Outline each Plasmodium falciparum-infected red blood cell.
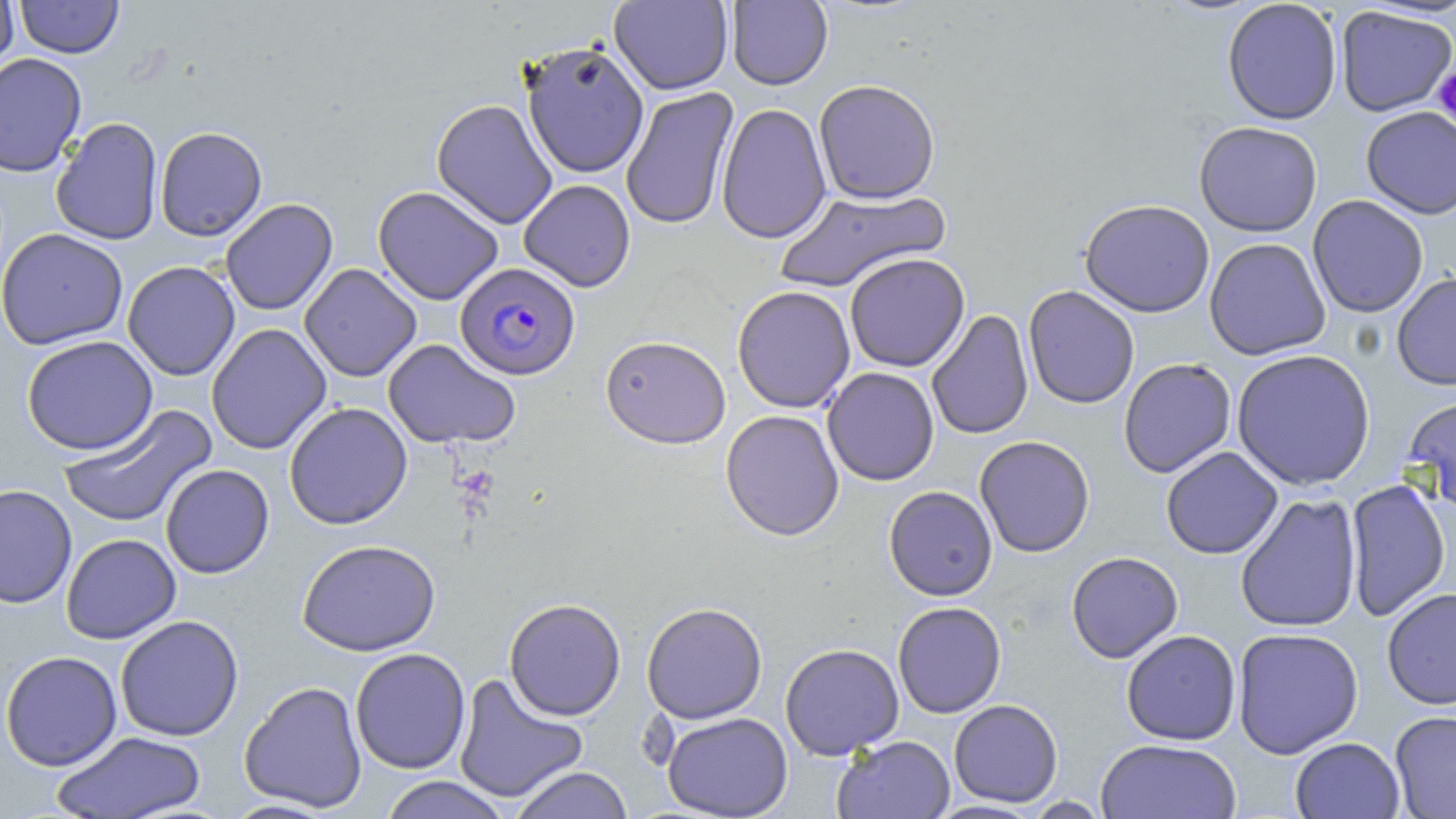
Approximate bounding boxes as named x1/y1/x2/y2 corners in pixels.
Plasmodium falciparum-infected red blood cells: (x1=456, y1=262, x2=581, y2=380).

Uninfected red blood cell locations: (x1=0, y1=0, x2=18, y2=77), (x1=15, y1=0, x2=124, y2=59), (x1=609, y1=0, x2=733, y2=95), (x1=726, y1=0, x2=833, y2=90), (x1=1222, y1=0, x2=1343, y2=125), (x1=1335, y1=6, x2=1456, y2=117), (x1=521, y1=41, x2=649, y2=179), (x1=0, y1=53, x2=87, y2=177), (x1=813, y1=78, x2=941, y2=203), (x1=621, y1=87, x2=739, y2=230), (x1=431, y1=98, x2=558, y2=229), (x1=716, y1=103, x2=832, y2=244), (x1=1361, y1=106, x2=1456, y2=219), (x1=50, y1=117, x2=164, y2=246), (x1=1194, y1=121, x2=1323, y2=236), (x1=154, y1=126, x2=267, y2=241), (x1=518, y1=178, x2=636, y2=292), (x1=373, y1=186, x2=503, y2=305), (x1=774, y1=187, x2=951, y2=293), (x1=1307, y1=195, x2=1429, y2=317), (x1=220, y1=198, x2=338, y2=316), (x1=1079, y1=198, x2=1215, y2=318), (x1=0, y1=228, x2=129, y2=350), (x1=1204, y1=238, x2=1331, y2=360), (x1=844, y1=253, x2=970, y2=372), (x1=122, y1=260, x2=240, y2=381), (x1=299, y1=263, x2=421, y2=382), (x1=1392, y1=272, x2=1456, y2=390), (x1=732, y1=285, x2=856, y2=413), (x1=1023, y1=286, x2=1140, y2=409), (x1=926, y1=309, x2=1034, y2=441), (x1=206, y1=323, x2=332, y2=454), (x1=600, y1=334, x2=731, y2=449), (x1=21, y1=335, x2=158, y2=455), (x1=383, y1=339, x2=521, y2=449), (x1=1231, y1=349, x2=1376, y2=491), (x1=1118, y1=358, x2=1236, y2=478), (x1=822, y1=367, x2=939, y2=486), (x1=1405, y1=393, x2=1456, y2=515), (x1=284, y1=402, x2=412, y2=530), (x1=56, y1=404, x2=218, y2=530), (x1=720, y1=410, x2=844, y2=540), (x1=974, y1=435, x2=1095, y2=557), (x1=1160, y1=447, x2=1283, y2=559), (x1=160, y1=464, x2=275, y2=578), (x1=1344, y1=479, x2=1451, y2=623), (x1=0, y1=484, x2=77, y2=609), (x1=884, y1=485, x2=998, y2=601), (x1=1234, y1=493, x2=1363, y2=633), (x1=61, y1=533, x2=181, y2=644), (x1=297, y1=538, x2=441, y2=656), (x1=1066, y1=551, x2=1183, y2=663), (x1=1381, y1=588, x2=1456, y2=710), (x1=504, y1=598, x2=626, y2=721), (x1=892, y1=601, x2=1006, y2=718), (x1=641, y1=602, x2=768, y2=723), (x1=115, y1=615, x2=244, y2=741), (x1=1231, y1=627, x2=1364, y2=759), (x1=1121, y1=630, x2=1241, y2=745), (x1=779, y1=643, x2=904, y2=759), (x1=350, y1=648, x2=471, y2=774), (x1=1, y1=650, x2=122, y2=771), (x1=452, y1=673, x2=589, y2=804), (x1=239, y1=680, x2=367, y2=812), (x1=949, y1=699, x2=1063, y2=807), (x1=1389, y1=710, x2=1456, y2=818), (x1=661, y1=712, x2=793, y2=818), (x1=51, y1=730, x2=207, y2=819), (x1=832, y1=735, x2=955, y2=819), (x1=1290, y1=737, x2=1405, y2=819), (x1=1095, y1=738, x2=1242, y2=819), (x1=509, y1=766, x2=634, y2=819), (x1=378, y1=776, x2=511, y2=819). Platelet locations: (x1=1433, y1=65, x2=1456, y2=127). Slide-level diagnosis: Plasmodium falciparum. Captured at 1000x magnification. Image is 1456×819 pixels. Light microscopy. Thin blood film. May-Grünwald-Giemsa-stained preparation. One field of a larger specimen.